Classify this cell by malaria status.
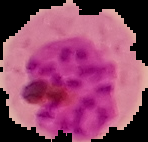

Parasitized.

Summary:
  - Preparation: thin blood film
  - Image size: 148×142 pixels
  - Image type: segmented cell region with the area outside set to black